State the blood parasite species.
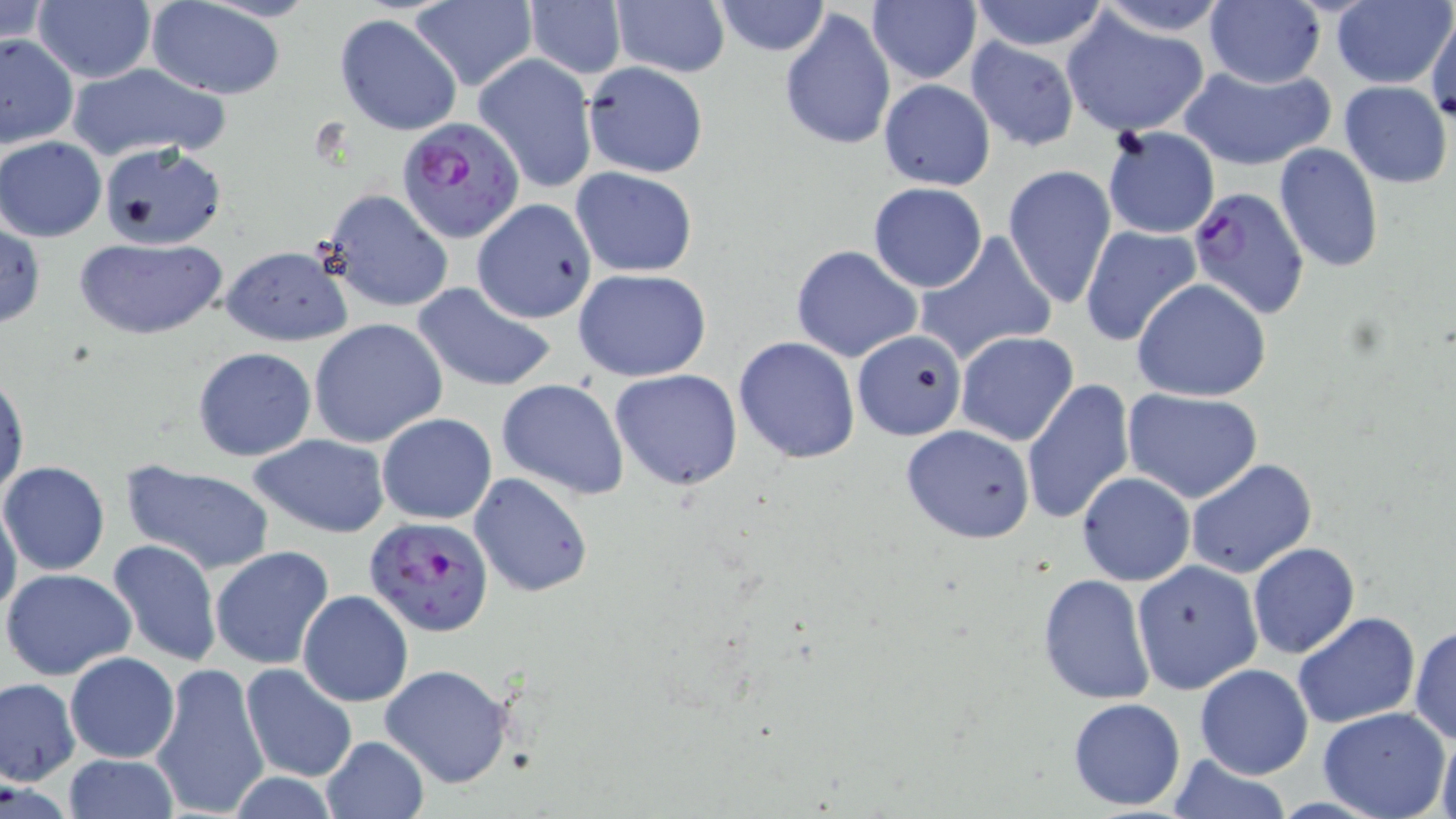

Plasmodium falciparum.

Summary:
  - Coordinate format: approximate bounding boxes as named x1/y1/x2/y2 corners in pixels
  - Plasmodium falciparum-infected red blood cell locations: (x1=398, y1=118, x2=526, y2=243), (x1=1185, y1=185, x2=1311, y2=319), (x1=363, y1=515, x2=496, y2=637)
  - Uninfected red blood cell locations: (x1=146, y1=0, x2=290, y2=98), (x1=523, y1=0, x2=626, y2=80), (x1=712, y1=0, x2=830, y2=55), (x1=967, y1=0, x2=1113, y2=53), (x1=1088, y1=0, x2=1234, y2=35), (x1=1203, y1=0, x2=1325, y2=89), (x1=1332, y1=0, x2=1454, y2=89), (x1=406, y1=1, x2=536, y2=92), (x1=1, y1=2, x2=53, y2=54), (x1=33, y1=2, x2=156, y2=84), (x1=610, y1=2, x2=730, y2=79), (x1=867, y1=2, x2=981, y2=84), (x1=780, y1=9, x2=897, y2=152), (x1=1061, y1=10, x2=1212, y2=137), (x1=1426, y1=10, x2=1456, y2=124), (x1=334, y1=13, x2=463, y2=137), (x1=0, y1=32, x2=79, y2=151), (x1=964, y1=38, x2=1080, y2=152), (x1=473, y1=54, x2=599, y2=194), (x1=65, y1=61, x2=231, y2=161), (x1=581, y1=61, x2=709, y2=178), (x1=1177, y1=63, x2=1335, y2=170), (x1=878, y1=79, x2=995, y2=192), (x1=1338, y1=82, x2=1452, y2=187), (x1=1102, y1=126, x2=1219, y2=240), (x1=1, y1=137, x2=106, y2=242), (x1=98, y1=141, x2=228, y2=249), (x1=1272, y1=143, x2=1385, y2=274), (x1=1003, y1=164, x2=1117, y2=310), (x1=571, y1=167, x2=698, y2=277), (x1=868, y1=183, x2=988, y2=293), (x1=320, y1=189, x2=456, y2=313), (x1=470, y1=199, x2=598, y2=324), (x1=0, y1=223, x2=46, y2=328), (x1=1080, y1=225, x2=1202, y2=346), (x1=914, y1=231, x2=1057, y2=364), (x1=77, y1=236, x2=226, y2=340), (x1=791, y1=244, x2=924, y2=361), (x1=219, y1=245, x2=351, y2=346), (x1=573, y1=269, x2=713, y2=382), (x1=1133, y1=278, x2=1272, y2=402), (x1=411, y1=281, x2=558, y2=392), (x1=310, y1=318, x2=447, y2=448), (x1=852, y1=328, x2=967, y2=439), (x1=955, y1=331, x2=1079, y2=446), (x1=733, y1=336, x2=860, y2=464), (x1=192, y1=347, x2=317, y2=462), (x1=610, y1=368, x2=743, y2=491), (x1=1, y1=374, x2=28, y2=499), (x1=497, y1=379, x2=629, y2=500), (x1=1023, y1=380, x2=1138, y2=527), (x1=1122, y1=388, x2=1263, y2=502), (x1=378, y1=412, x2=496, y2=524), (x1=900, y1=423, x2=1035, y2=543), (x1=248, y1=434, x2=390, y2=537), (x1=1185, y1=457, x2=1317, y2=579), (x1=0, y1=461, x2=110, y2=576), (x1=122, y1=461, x2=275, y2=574), (x1=1076, y1=470, x2=1196, y2=587), (x1=469, y1=472, x2=595, y2=598), (x1=5, y1=485, x2=41, y2=605), (x1=0, y1=494, x2=22, y2=622), (x1=105, y1=537, x2=222, y2=668), (x1=1248, y1=543, x2=1360, y2=658), (x1=210, y1=545, x2=335, y2=671), (x1=1130, y1=560, x2=1263, y2=694), (x1=2, y1=568, x2=136, y2=680), (x1=1037, y1=573, x2=1156, y2=706), (x1=298, y1=590, x2=414, y2=707), (x1=1292, y1=611, x2=1420, y2=729), (x1=1409, y1=625, x2=1456, y2=745), (x1=64, y1=650, x2=180, y2=762), (x1=150, y1=660, x2=270, y2=819), (x1=380, y1=663, x2=516, y2=789), (x1=1195, y1=663, x2=1314, y2=780), (x1=241, y1=664, x2=357, y2=783), (x1=0, y1=677, x2=81, y2=785), (x1=1067, y1=697, x2=1187, y2=813), (x1=1318, y1=707, x2=1452, y2=819), (x1=1432, y1=729, x2=1456, y2=817), (x1=320, y1=735, x2=430, y2=819), (x1=63, y1=755, x2=179, y2=817), (x1=1164, y1=756, x2=1294, y2=817)
  - Modality: optical microscopy
  - Field of view: one of a larger specimen
  - Magnification: 1000x
  - Image size: 1456×819 pixels
  - Preparation: thin blood smear
  - Stain: May-Grünwald-Giemsa